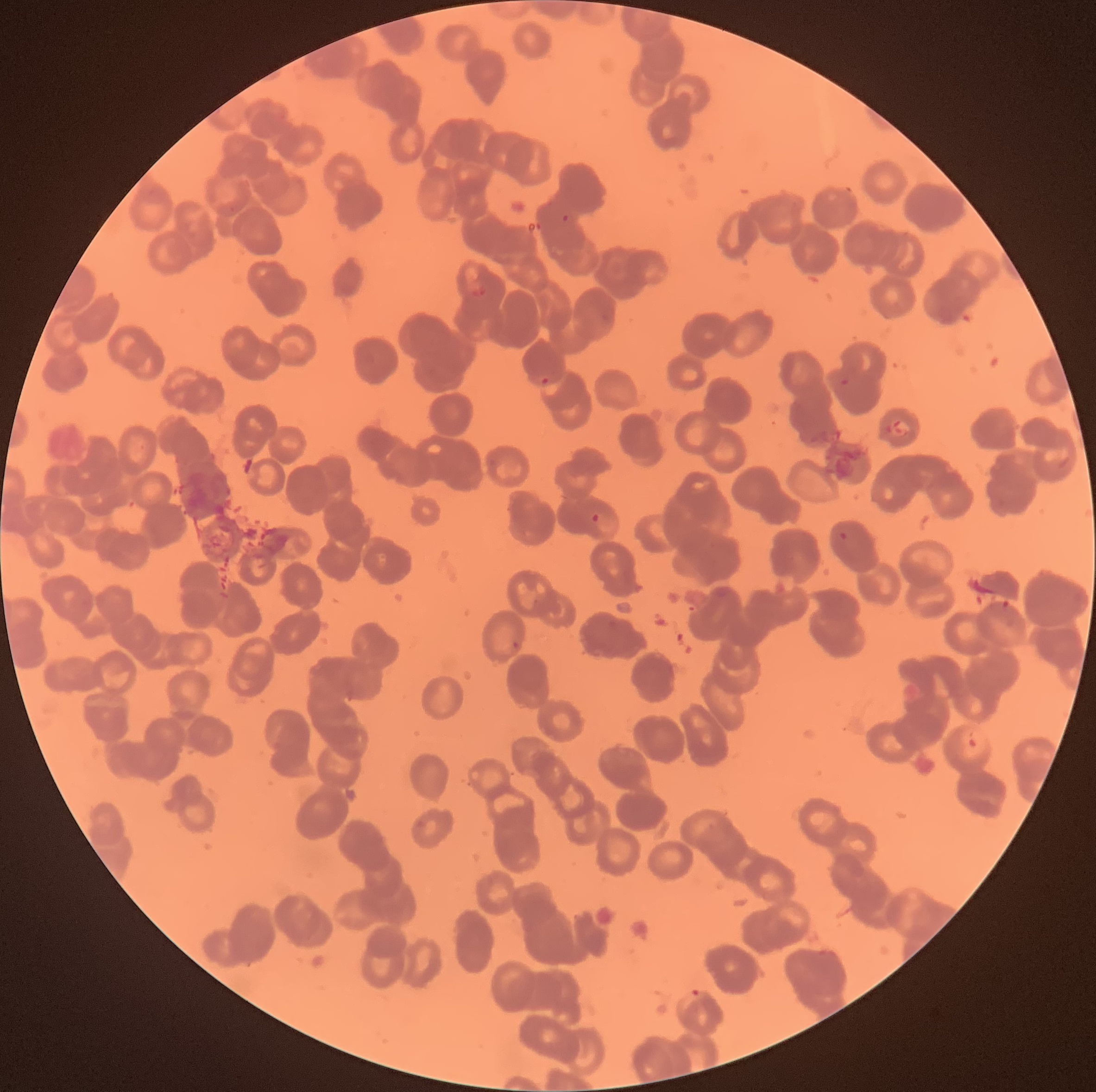 Approximate bounding boxes as named x1/y1/x2/y2 corners in pixels. Plasmodium parasite locations: (x1=840, y1=186, x2=854, y2=195), (x1=226, y1=203, x2=239, y2=213), (x1=562, y1=212, x2=569, y2=222), (x1=468, y1=279, x2=487, y2=298), (x1=530, y1=374, x2=551, y2=385), (x1=837, y1=376, x2=851, y2=386), (x1=590, y1=512, x2=601, y2=524), (x1=838, y1=532, x2=849, y2=541), (x1=510, y1=640, x2=520, y2=650), (x1=962, y1=730, x2=986, y2=758), (x1=678, y1=989, x2=704, y2=1008). Thin blood film. Image is 1096×1092 pixels. Light microscopy. The red blood cells show rouleaux formation.